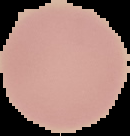
{
  "image_size": "130×136 pixels",
  "preparation": "thin blood film",
  "image_type": "cell region segmented out of the field of view; surrounding area masked to black",
  "result": "no malaria parasites seen"
}